Locate every Plasmodium falciparum-infected red blood cell.
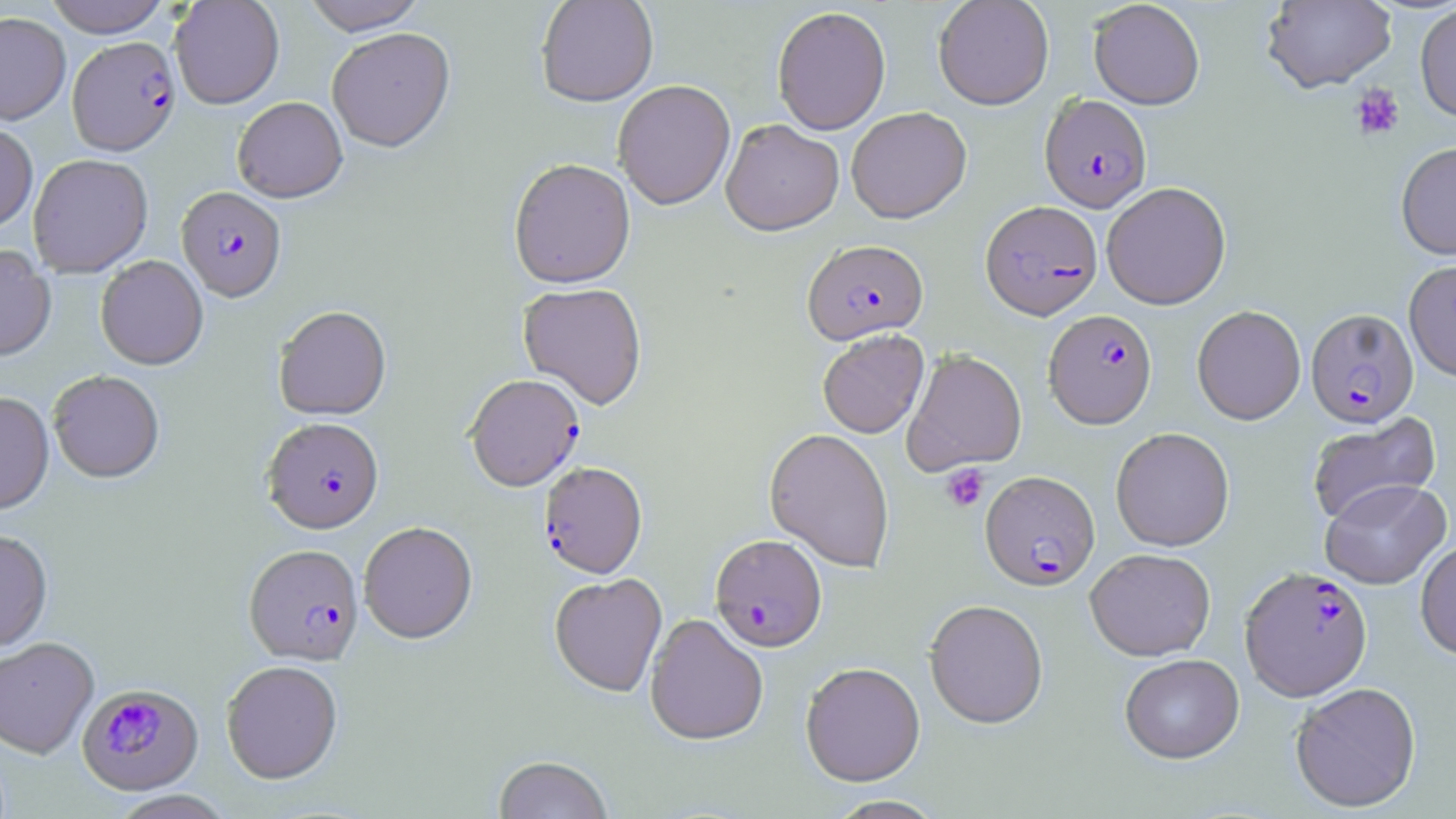

Approximate bounding boxes as (x1,y1)-(x2,y2) corner pairs in pixels.
Plasmodium falciparum-infected red blood cells: (67,37)-(181,158), (1040,93)-(1152,212), (175,188)-(287,305), (981,200)-(1103,320), (802,239)-(928,345), (1306,308)-(1419,428), (1043,310)-(1157,428), (464,376)-(585,493), (262,420)-(384,537), (538,463)-(648,581), (980,470)-(1099,591), (710,534)-(827,654), (243,547)-(364,668), (1240,566)-(1373,701), (77,685)-(205,797).

slide_level_diagnosis: Plasmodium falciparum
uninfected_red_blood_cell_locations: 'approximate bounding boxes as (x1,y1)-(x2,y2) corner pairs in pixels: (43,0)-(172,38), (169,0)-(285,111), (302,0)-(427,37), (535,0)-(658,109), (933,0)-(1054,110), (1261,0)-(1396,94), (1088,1)-(1205,109), (1414,3)-(1456,123), (772,6)-(891,135), (0,12)-(71,125), (326,30)-(456,155), (613,80)-(735,212), (232,98)-(347,205), (846,107)-(971,223), (721,120)-(844,236), (0,123)-(38,236), (1395,141)-(1456,260), (28,156)-(154,278), (509,161)-(636,292), (1101,181)-(1231,309), (0,246)-(57,364), (96,257)-(208,372), (1404,259)-(1456,382), (517,284)-(648,411), (1192,305)-(1306,425), (273,308)-(392,422), (817,329)-(929,438), (903,349)-(1027,475), (48,373)-(164,486), (0,394)-(54,518), (1307,413)-(1440,528), (1110,427)-(1235,551), (764,428)-(895,572), (1320,479)-(1450,589), (359,524)-(478,647), (0,532)-(53,654), (1415,538)-(1456,661), (1085,548)-(1216,661), (549,574)-(667,699), (924,599)-(1048,729), (645,614)-(769,747), (0,638)-(99,760), (1120,653)-(1244,763), (800,662)-(926,786), (221,663)-(343,786), (1290,681)-(1422,812), (494,757)-(613,819), (108,791)-(237,819), (826,795)-(947,818)'
modality: light microscopy
magnification: 1000x
field_of_view: one of a larger specimen
preparation: thin blood film
image_size: 1456×819 pixels
stain: May-Grünwald-Giemsa
platelet_locations: 'approximate bounding boxes as (x1,y1)-(x2,y2) corner pairs in pixels: (1350,84)-(1404,141), (940,464)-(989,512)'